Outline each Plasmodium falciparum-infected red blood cell.
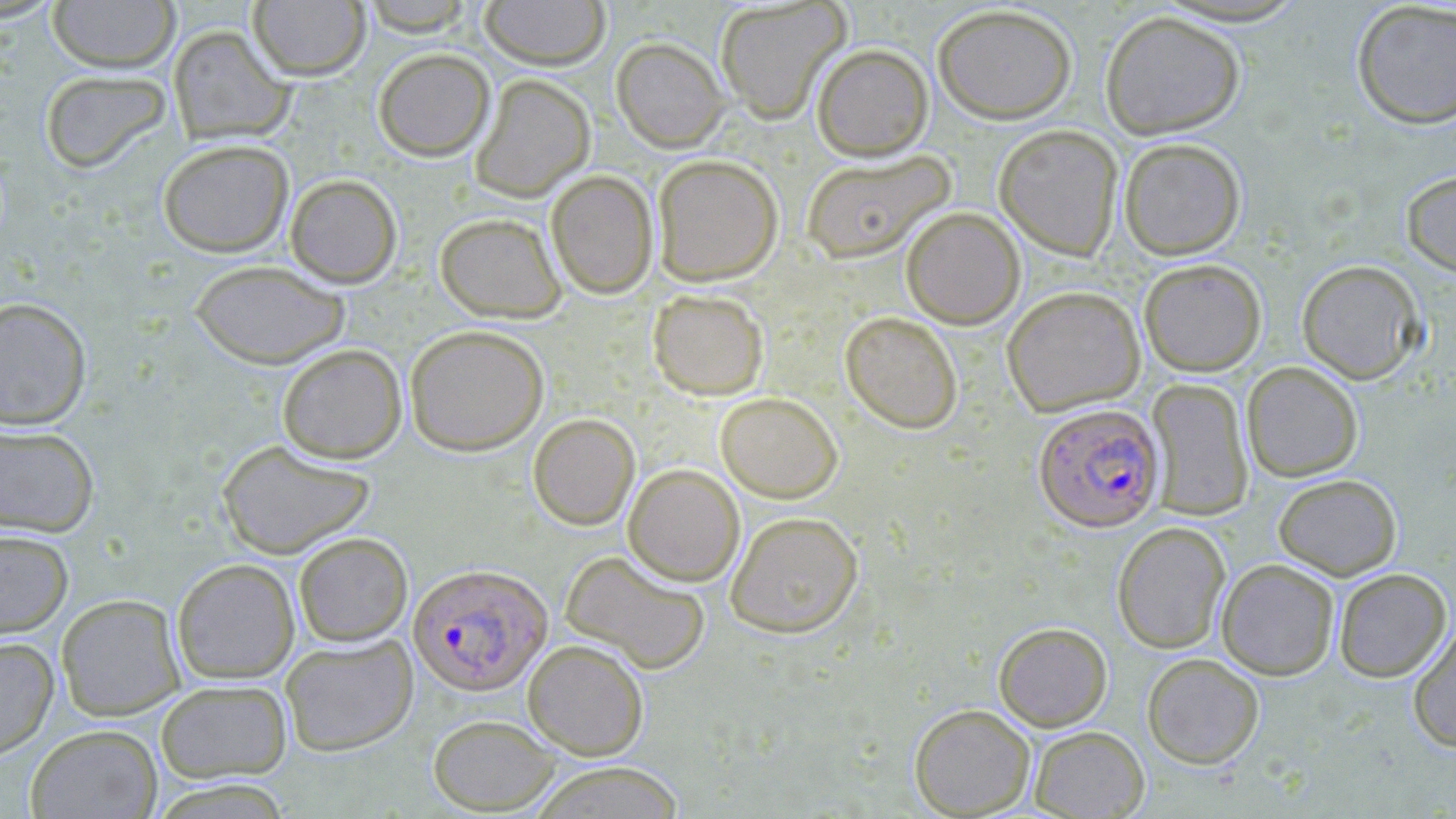

Approximate bounding boxes as (x1, y1, x2, y2) in pixels.
Plasmodium falciparum-infected red blood cells: (1033, 402, 1165, 532), (408, 563, 552, 696).

slide-level diagnosis = Plasmodium falciparum
modality = optical microscopy
image size = 1456×819 pixels
stain = May-Grünwald-Giemsa
field of view = single
preparation = thin blood film
uninfected red blood cell locations = approximate bounding boxes as (x1, y1, x2, y2) in pixels: (47, 0, 180, 73), (479, 0, 610, 70), (714, 0, 850, 123), (249, 1, 371, 80), (359, 1, 478, 36), (1351, 1, 1456, 129), (932, 4, 1077, 124), (1100, 9, 1245, 139), (168, 25, 294, 145), (611, 37, 729, 152), (811, 43, 934, 161), (373, 48, 495, 162), (39, 69, 172, 174), (469, 73, 596, 202), (994, 124, 1124, 261), (1118, 137, 1247, 260), (157, 138, 294, 258), (801, 150, 955, 264), (652, 153, 784, 286), (546, 170, 658, 299), (1401, 170, 1456, 277), (284, 173, 403, 288), (901, 207, 1025, 329), (434, 212, 567, 323), (1138, 258, 1266, 377), (190, 259, 349, 369), (1296, 259, 1426, 384), (1002, 285, 1145, 416), (647, 288, 769, 401), (0, 296, 92, 430), (840, 311, 963, 433), (404, 324, 550, 456), (277, 343, 407, 463), (1241, 361, 1364, 482), (1145, 378, 1254, 521), (715, 392, 843, 503), (528, 413, 640, 530), (0, 422, 100, 538), (216, 439, 376, 559), (623, 463, 745, 586), (1273, 473, 1402, 580), (724, 510, 864, 638), (1112, 521, 1231, 654), (0, 529, 73, 637), (293, 532, 413, 647), (560, 550, 711, 675), (172, 558, 300, 684), (1216, 559, 1340, 680), (1333, 567, 1452, 682), (56, 593, 185, 721), (1408, 620, 1456, 752), (994, 622, 1112, 730), (0, 636, 59, 759), (280, 636, 418, 756), (523, 639, 649, 760), (1142, 652, 1264, 769), (155, 679, 292, 784), (909, 703, 1035, 817), (427, 713, 561, 814), (25, 724, 163, 819), (1029, 726, 1149, 818), (526, 761, 688, 818)
magnification = 1000x